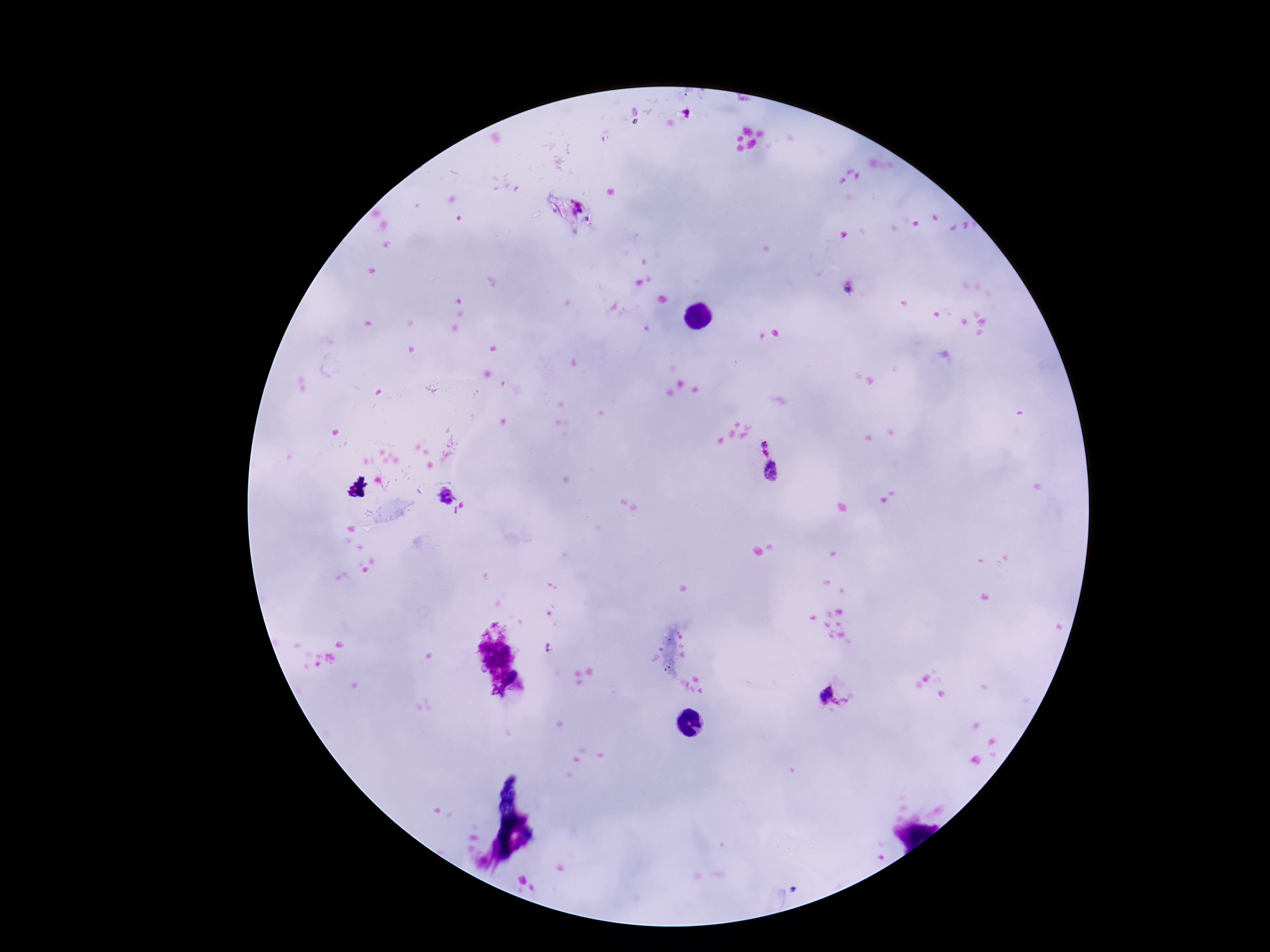
Approximate centers as [x, y] in pixels. Plasmodium parasite locations: [852, 288], [765, 448], [772, 472], [445, 495], [825, 696]. Giemsa stain. One field from this slide. Smartphone photograph taken through the microscope eyepiece. Thick blood smear. 100x magnification. Image is 1270×952 pixels. Patient malaria status: infected.